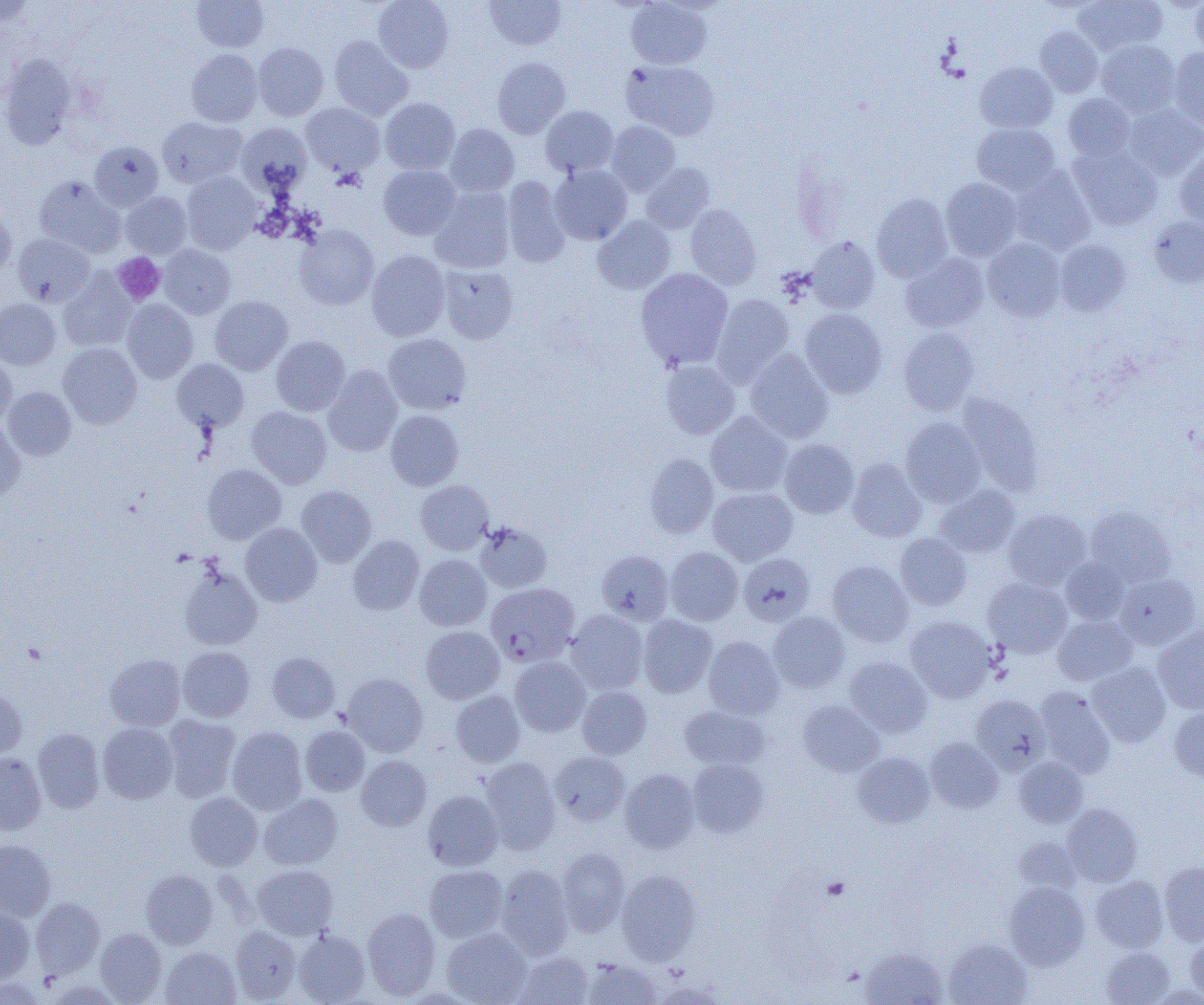 Approximate bounding boxes as (x1,y1)-(x2,y2) corner pairs in pixels. Uninfected red blood cell locations: (0,0)-(39,27), (372,0)-(454,73), (484,0)-(566,51), (626,0)-(712,69), (1073,0)-(1166,56), (1191,0)-(1204,54), (192,1)-(269,52), (1035,27)-(1103,97), (329,35)-(413,121), (1096,39)-(1181,116), (253,42)-(328,120), (1168,47)-(1204,130), (186,49)-(262,127), (1,55)-(79,150), (492,57)-(570,139), (621,59)-(719,140), (975,61)-(1057,133), (1063,93)-(1136,161), (379,97)-(460,175), (301,102)-(385,176), (1122,103)-(1204,180), (540,105)-(619,177), (156,117)-(246,187), (606,121)-(680,196), (236,122)-(312,195), (971,123)-(1061,195), (444,124)-(520,197), (89,141)-(163,211), (1069,145)-(1163,231), (1174,147)-(1204,230), (640,162)-(715,234), (549,164)-(632,245), (378,165)-(461,240), (1009,165)-(1096,255), (182,171)-(262,254), (34,175)-(125,257), (502,176)-(570,268), (940,178)-(1022,261), (429,187)-(515,273), (120,191)-(192,259), (871,193)-(953,282), (0,202)-(16,276), (685,204)-(761,289), (592,215)-(676,295), (1147,216)-(1204,288), (294,225)-(379,310), (12,234)-(95,306), (805,236)-(880,314), (982,238)-(1066,321), (1054,239)-(1131,317), (158,244)-(236,319), (366,249)-(450,341), (901,253)-(989,332), (438,265)-(519,344), (635,268)-(733,371), (58,269)-(137,352), (711,294)-(794,386), (210,295)-(293,375), (0,298)-(60,369), (121,299)-(198,383), (800,309)-(887,399), (898,327)-(980,416), (383,333)-(471,414), (271,336)-(350,416), (58,342)-(142,429), (745,348)-(833,443), (0,354)-(17,425), (172,358)-(249,432), (661,360)-(740,440), (324,365)-(403,456), (2,386)-(76,460), (956,393)-(1043,494), (247,406)-(332,488), (386,410)-(464,490), (705,411)-(793,497), (0,416)-(25,500), (900,417)-(986,507), (779,438)-(859,519), (644,453)-(718,538), (847,457)-(927,542), (202,464)-(286,543), (415,480)-(493,555), (296,485)-(376,567), (934,485)-(1020,558), (708,487)-(798,565), (1085,506)-(1176,587), (1003,509)-(1091,590), (475,521)-(552,592), (240,523)-(322,606), (895,533)-(972,610), (348,535)-(424,615), (665,546)-(743,625), (596,550)-(674,625), (739,553)-(815,626), (414,554)-(492,631), (1061,557)-(1131,626), (827,560)-(913,647), (179,566)-(262,650), (1114,572)-(1202,650), (983,577)-(1072,658), (567,609)-(649,694), (769,611)-(850,693), (638,614)-(717,697), (1053,615)-(1138,686), (905,616)-(997,703), (420,625)-(505,703), (1153,626)-(1204,714), (703,636)-(784,719), (178,646)-(255,722), (267,652)-(340,723), (105,653)-(185,730), (509,656)-(590,736), (845,657)-(932,737), (1087,662)-(1171,747), (342,672)-(428,757), (0,685)-(27,759), (577,686)-(652,759), (1034,687)-(1116,778), (451,690)-(525,767), (970,694)-(1050,774), (798,700)-(884,776), (678,705)-(770,771), (1168,706)-(1204,782), (162,714)-(241,802), (98,723)-(178,804), (300,726)-(370,796), (33,727)-(105,813), (227,727)-(308,814), (925,737)-(1004,813), (550,751)-(630,826), (0,752)-(47,834), (853,752)-(935,828), (356,755)-(431,831), (480,757)-(561,855), (1013,757)-(1088,828), (687,758)-(769,837), (620,768)-(700,853), (423,790)-(503,870), (185,792)-(263,870), (259,793)-(343,869), (1063,803)-(1143,887), (1013,836)-(1082,895), (0,840)-(56,920), (556,847)-(630,936), (1159,861)-(1204,945), (252,864)-(338,939), (424,864)-(509,942), (496,865)-(574,959), (141,869)-(218,948), (616,869)-(701,964), (1092,875)-(1169,952), (1004,881)-(1090,969), (31,897)-(105,979), (0,906)-(36,983), (362,907)-(441,999), (231,924)-(302,1003), (441,927)-(531,1005), (95,928)-(167,1003), (293,930)-(370,1004), (1185,933)-(1204,1002), (943,938)-(1032,1005), (160,946)-(240,1005), (1100,946)-(1176,1005), (860,947)-(947,1005), (512,951)-(594,1005), (582,958)-(662,1004). Platelet locations: (112,252)-(165,305), (22,642)-(47,664), (822,877)-(850,900). Plasmodium falciparum-infected red blood cell locations: (486,583)-(580,666). Slide-level diagnosis: Plasmodium falciparum. 1000x magnification. Single field of view. Light microscopy. Thin blood film. Image is 1204×1005 pixels.